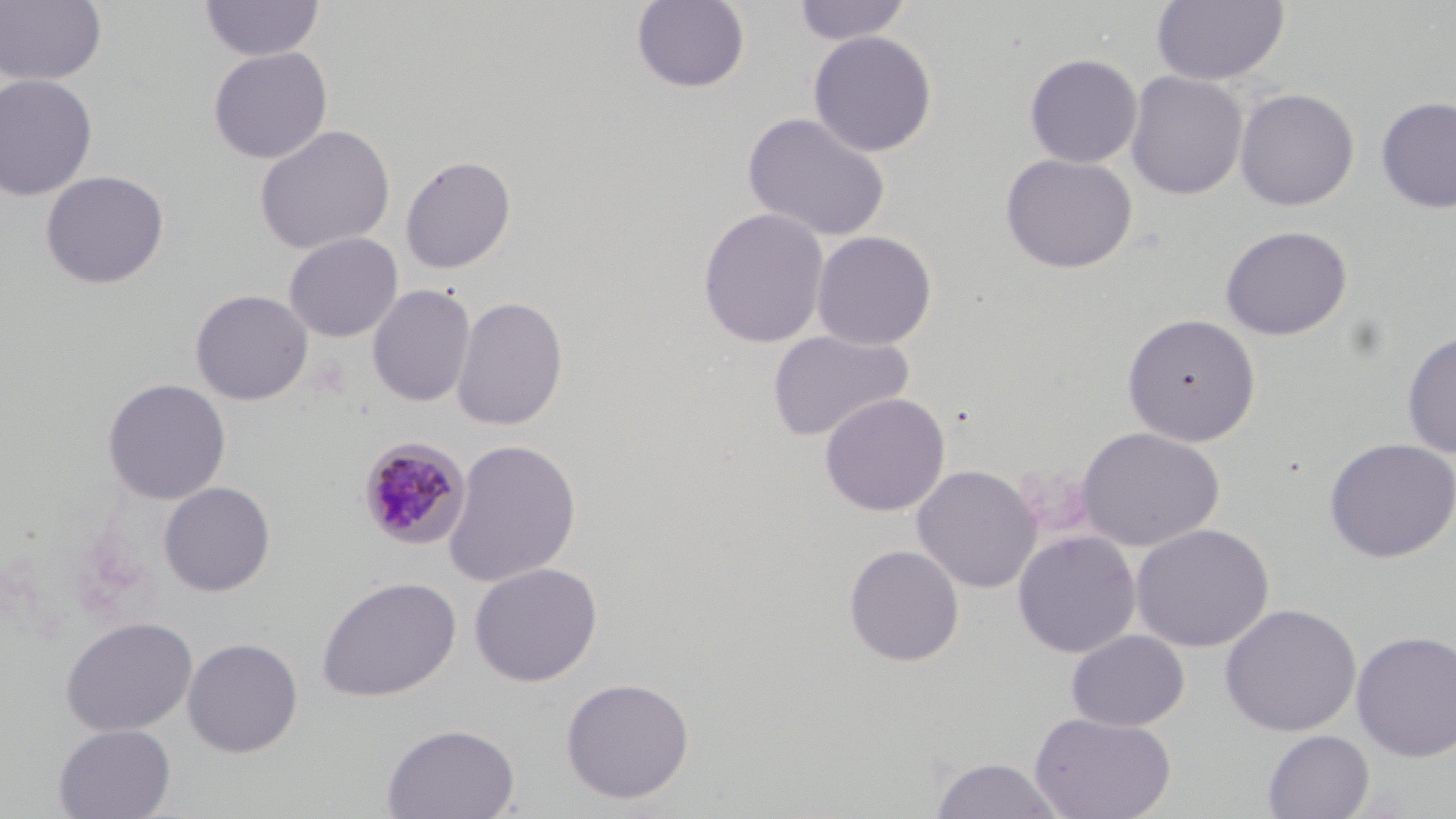
Approximate bounding boxes as (x1,y1)-(x2,y2) corner pairs in pixels. Uninfected red blood cell locations: (0,0)-(108,87), (199,0)-(326,62), (631,0)-(751,94), (792,0)-(913,46), (1150,0)-(1290,86), (808,30)-(937,157), (208,47)-(332,164), (1024,53)-(1142,168), (1124,70)-(1248,200), (0,73)-(98,201), (1235,87)-(1359,211), (1375,96)-(1456,214), (742,111)-(891,243), (254,124)-(395,255), (1000,153)-(1138,273), (400,155)-(517,274), (40,170)-(169,290), (697,207)-(829,348), (1220,225)-(1353,340), (811,230)-(937,350), (284,232)-(403,342), (367,283)-(476,408), (190,289)-(313,405), (451,295)-(569,431), (1122,313)-(1261,446), (767,329)-(915,443), (1401,329)-(1456,458), (102,377)-(231,505), (820,392)-(950,517), (1076,426)-(1225,551), (1323,437)-(1456,563), (443,438)-(582,587), (912,464)-(1041,594), (158,481)-(275,597), (1130,523)-(1274,653), (1012,530)-(1141,658), (843,544)-(964,666), (469,562)-(602,687), (317,575)-(461,702), (1219,603)-(1361,737), (60,617)-(198,736), (1066,630)-(1190,732), (1351,630)-(1456,763), (182,636)-(304,757), (560,677)-(695,804), (1029,712)-(1177,819), (53,723)-(176,818), (382,723)-(520,819), (1262,729)-(1374,819), (929,756)-(1066,818). Plasmodium malariae-infected red blood cell locations: (358,436)-(471,550). Slide-level diagnosis: Plasmodium malariae. May-Grünwald-Giemsa-stained preparation. Optical microscopy. Image is 1456×819 pixels. 1000x magnification. One field of a larger specimen. Thin blood film.